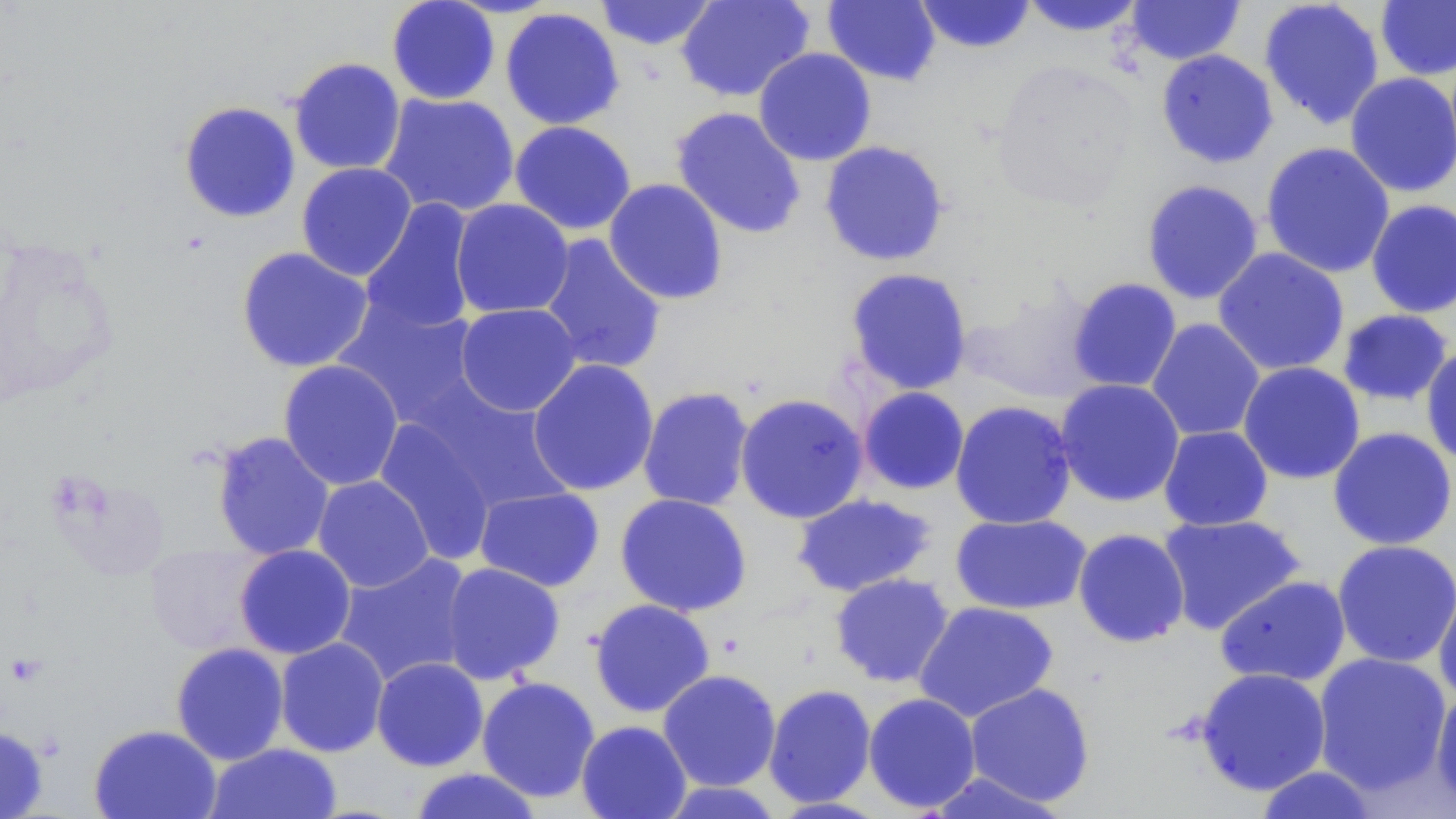

Approximate bounding boxes as [x1, y1, x2, y2] in pixels. Uninfected red blood cell locations: [386, 0, 500, 105], [595, 0, 719, 51], [675, 0, 815, 102], [822, 0, 941, 87], [913, 0, 1037, 54], [1258, 0, 1385, 129], [1018, 1, 1147, 37], [1124, 1, 1245, 65], [1375, 1, 1456, 81], [499, 7, 625, 130], [753, 47, 877, 166], [1156, 49, 1279, 168], [288, 57, 407, 175], [1344, 72, 1456, 198], [377, 92, 520, 218], [178, 101, 301, 223], [670, 106, 807, 240], [509, 120, 637, 235], [819, 140, 950, 267], [1260, 142, 1395, 278], [296, 163, 417, 282], [604, 178, 728, 305], [1141, 179, 1264, 305], [360, 198, 479, 335], [450, 198, 575, 319], [1366, 199, 1456, 318], [538, 234, 667, 376], [236, 246, 375, 373], [1212, 247, 1350, 377], [844, 267, 973, 395], [1067, 277, 1183, 393], [958, 282, 1105, 403], [333, 296, 484, 430], [454, 302, 582, 417], [1336, 309, 1455, 407], [1146, 318, 1266, 442], [1420, 344, 1456, 468], [527, 359, 659, 496], [278, 360, 404, 491], [1238, 362, 1365, 485], [1054, 379, 1185, 507], [407, 382, 574, 519], [638, 386, 755, 512], [857, 386, 970, 495], [734, 393, 869, 524], [950, 400, 1077, 530], [372, 416, 501, 565], [1158, 425, 1273, 531], [1327, 427, 1456, 551], [211, 431, 335, 560], [312, 475, 434, 592], [474, 487, 605, 592], [615, 493, 752, 617], [791, 493, 936, 597], [950, 513, 1092, 615], [1157, 513, 1306, 635], [1072, 528, 1190, 647], [1332, 539, 1456, 669], [146, 545, 270, 655], [234, 545, 356, 659], [333, 552, 477, 688], [440, 562, 566, 685], [829, 573, 955, 688], [1215, 575, 1351, 687], [1433, 580, 1456, 705], [588, 598, 715, 718], [914, 601, 1059, 722], [274, 637, 389, 757], [170, 642, 289, 765], [1311, 652, 1452, 797], [371, 657, 489, 772], [1195, 667, 1331, 796], [657, 669, 781, 792], [476, 676, 601, 802], [964, 682, 1095, 807], [763, 684, 877, 809], [1431, 685, 1456, 811], [862, 692, 982, 813], [576, 720, 691, 819], [89, 723, 222, 819], [0, 724, 48, 818], [205, 743, 343, 819], [1255, 765, 1380, 818], [408, 767, 544, 819], [922, 770, 1069, 818], [659, 780, 785, 819]. Slide-level diagnosis: negative for blood parasites. Thin blood film. May-Grünwald-Giemsa stain. Image is 1456×819 pixels. Optical microscopy. Single field of view. 1000x magnification.